State which parasite is depicted.
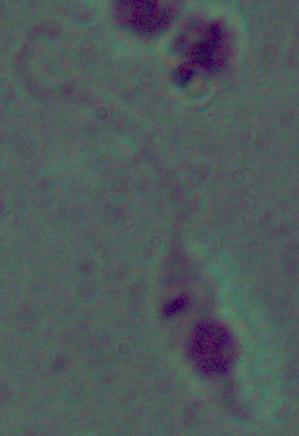
Leishmania.

Micrograph. Captured at 1000x magnification.